Name the parasite shown.
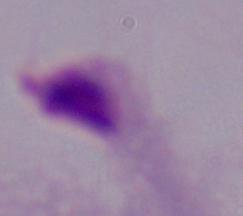

A trichomonad.

Summary:
  - Magnification: 1000x
  - Modality: micrograph